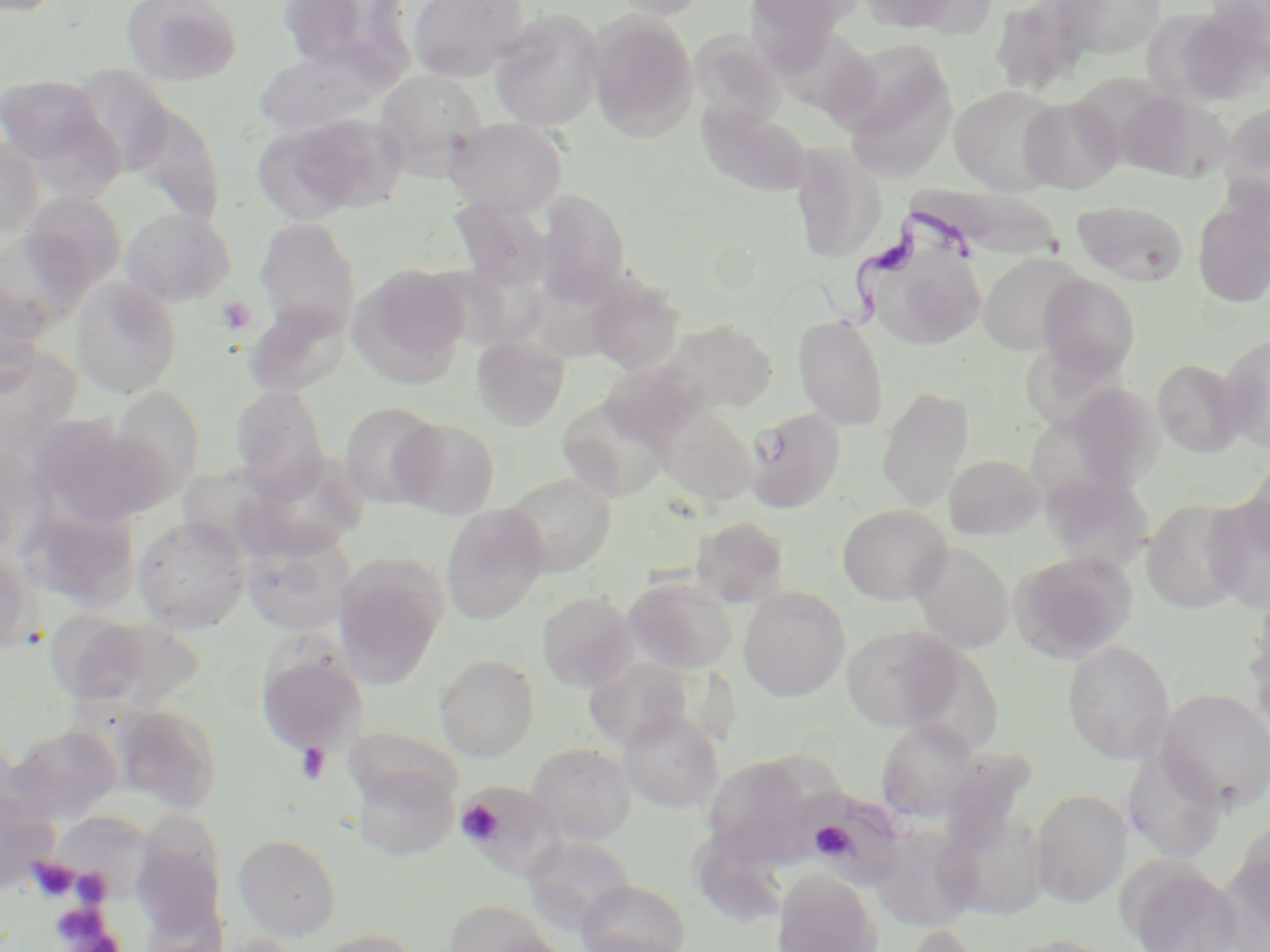

Summary:
  - Coordinate format: approximate bounding boxes as [x1, y1, x2, y2] in pixels
  - Trypanosoma brucei locations: [799, 207, 988, 338]
  - Uninfected red blood cell locations: [121, 0, 242, 87], [272, 0, 404, 72], [408, 0, 528, 82], [606, 0, 711, 19], [743, 0, 865, 53], [855, 0, 970, 33], [1053, 0, 1168, 59], [1206, 0, 1270, 55], [989, 1, 1096, 95], [1185, 4, 1270, 88], [489, 8, 605, 132], [589, 12, 698, 140], [689, 31, 785, 128], [254, 45, 388, 136], [840, 45, 959, 180], [68, 65, 175, 177], [374, 70, 488, 171], [0, 74, 111, 171], [949, 85, 1066, 194], [1117, 90, 1230, 183], [1019, 96, 1123, 193], [129, 101, 226, 224], [1218, 102, 1270, 211], [698, 103, 813, 197], [255, 115, 393, 222], [444, 118, 568, 218], [0, 137, 43, 242], [788, 143, 886, 264], [916, 186, 1085, 266], [534, 189, 632, 305], [21, 190, 127, 294], [450, 196, 554, 290], [1192, 197, 1270, 309], [1072, 199, 1187, 285], [120, 207, 235, 307], [254, 217, 361, 339], [865, 240, 987, 351], [978, 251, 1087, 354], [349, 264, 470, 387], [586, 273, 686, 374], [1037, 273, 1141, 381], [0, 274, 46, 394], [70, 276, 182, 398], [244, 303, 350, 397], [793, 315, 889, 430], [663, 317, 778, 415], [471, 335, 570, 430], [1218, 336, 1270, 452], [0, 345, 83, 465], [1152, 358, 1246, 457], [601, 359, 709, 449], [1065, 383, 1166, 494], [109, 386, 206, 498], [229, 386, 330, 498], [876, 386, 975, 512], [556, 399, 672, 503], [339, 402, 443, 508], [657, 405, 757, 506], [743, 407, 846, 513], [27, 415, 166, 526], [392, 417, 500, 518], [0, 446, 55, 555], [243, 452, 368, 559], [1243, 452, 1270, 561], [944, 454, 1045, 540], [503, 473, 616, 576], [1042, 473, 1152, 572], [1204, 494, 1270, 613], [1141, 498, 1251, 615], [21, 499, 139, 609], [440, 504, 549, 624], [837, 504, 951, 604], [132, 516, 250, 633], [690, 516, 792, 607], [240, 527, 356, 638], [911, 542, 1015, 653], [0, 549, 33, 656], [1011, 551, 1138, 662], [334, 555, 448, 686], [623, 576, 737, 674], [739, 587, 850, 702], [536, 591, 639, 692], [1243, 605, 1270, 741], [52, 612, 203, 713], [841, 624, 965, 731], [1063, 641, 1175, 764], [256, 646, 368, 756], [434, 654, 539, 761], [584, 656, 692, 750], [1157, 688, 1270, 812], [113, 704, 222, 814], [618, 709, 724, 814], [876, 719, 979, 821], [4, 725, 121, 824], [345, 728, 460, 812], [527, 742, 636, 844], [1122, 749, 1228, 863], [703, 754, 822, 861], [350, 761, 460, 861], [0, 788, 59, 894], [1031, 788, 1132, 908], [801, 791, 908, 889], [940, 804, 1048, 921], [54, 817, 160, 903], [1227, 823, 1270, 941], [868, 825, 978, 932], [132, 832, 228, 943], [233, 834, 342, 941], [521, 836, 637, 928], [1124, 863, 1243, 952], [772, 868, 882, 952], [575, 880, 690, 952], [442, 900, 561, 952], [308, 928, 423, 952], [1006, 933, 1120, 952]
  - Platelet locations: [217, 296, 256, 335], [296, 742, 332, 784], [455, 800, 504, 846], [810, 821, 856, 860], [27, 857, 79, 901], [71, 869, 110, 904], [48, 901, 120, 950]
  - Slide-level diagnosis: Trypanosoma brucei
  - Image size: 1270×952 pixels
  - Modality: light microscopy
  - Magnification: 1000x
  - Preparation: thin blood smear
  - Stain: May-Grünwald-Giemsa
  - Field of view: single